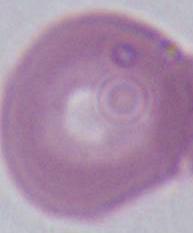
Summary:
  - Identification: erythrocyte
  - Modality: micrograph
  - Magnification: 1000x